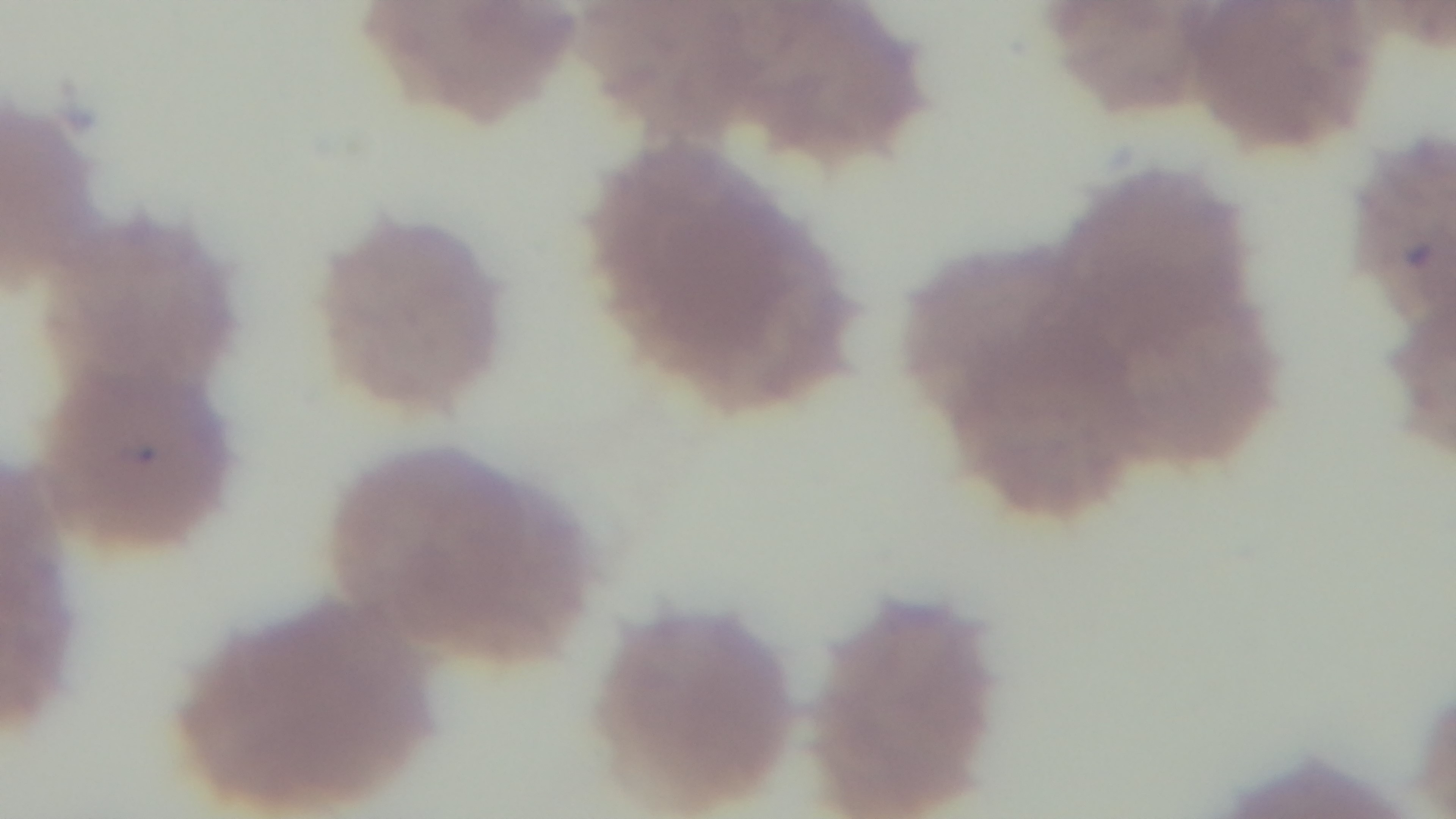
Mounted 4K digital camera. Preparation: thin blood film. Photomicrograph. Giemsa stain. 100x oil-immersion objective. Malaria status: positive. One field from the slide.